Classify this cell by malaria status.
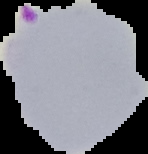
Parasitized.

Summary:
  - Image type: cell region segmented out of the field of view; surrounding area masked to black
  - Preparation: thin blood film
  - Image size: 148×154 pixels